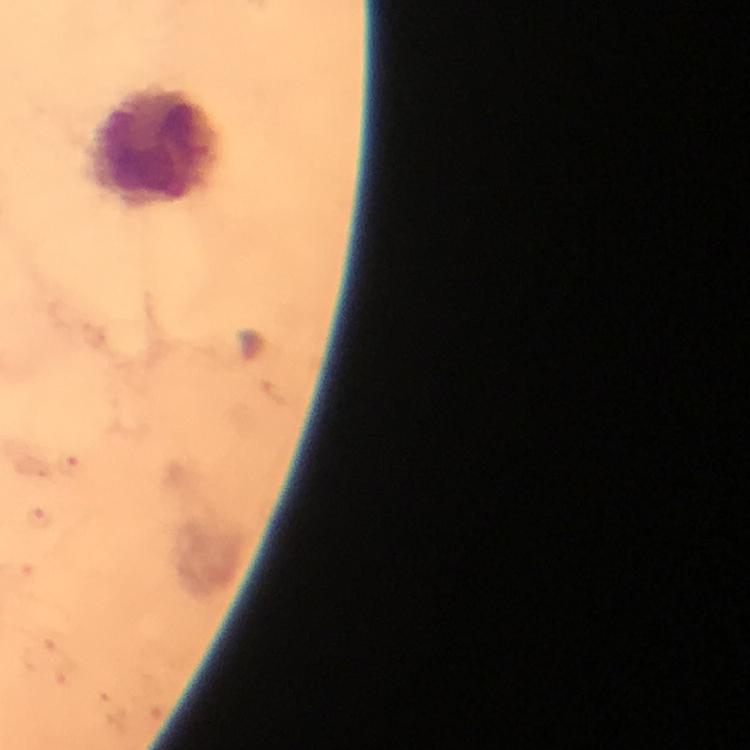

Approximate centers as [x, y] in pixels.
Summary:
  - Leukocyte locations: [154, 147]
  - Plasmodium parasites: none seen
  - Stain: Giemsa
  - Image size: 750×750 pixels
  - Preparation: thick blood smear
  - Capture: smartphone photograph through a microscope
  - Context: from a malaria diagnostic workup
  - Cropped from: one field of view
  - Immersion oil: applied
  - Magnification: 100x